Name the parasite shown.
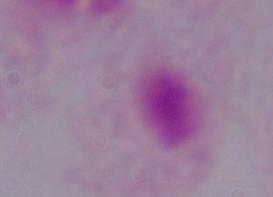

A trichomonad.

Summary:
  - Modality: micrograph
  - Magnification: 1000x